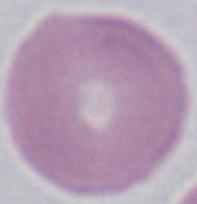

Summary:
  - Modality: photomicrograph
  - Magnification: 1000x
  - Identification: red blood cell